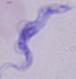

Summary:
  - Modality: photomicrograph
  - Magnification: 1000x
  - Identification: trypanosome